Outline each blood parasite and name the species.
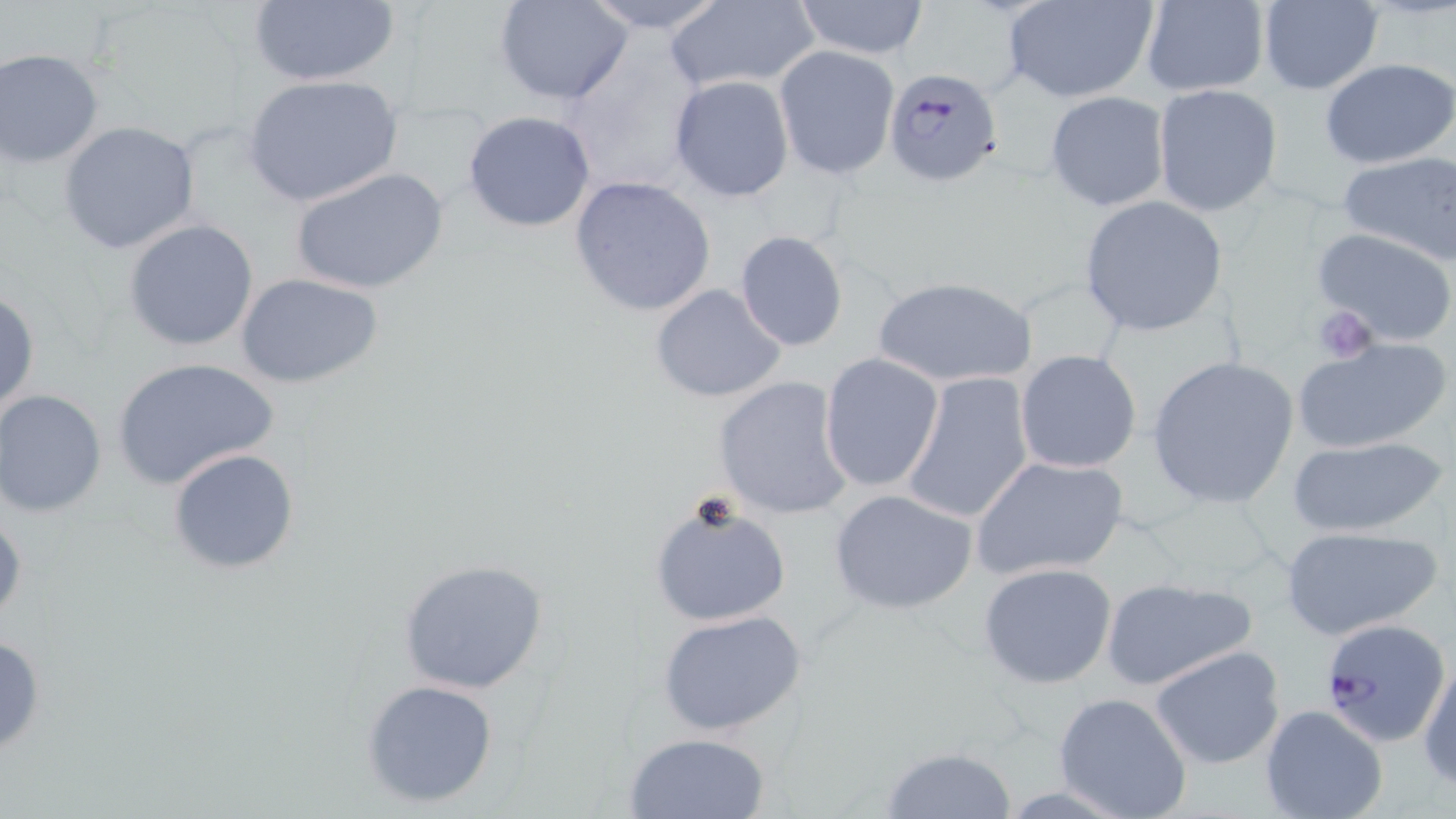

Approximate bounding boxes as (x1,y1)-(x2,y2) corner pairs in pixels.
Plasmodium falciparum-infected red blood cells: (882,66)-(1005,189), (1318,615)-(1449,745).
No Plasmodium ovale, Plasmodium malariae, Plasmodium vivax, Babesia divergens, or Trypanosoma brucei observed.

Uninfected red blood cell locations: (247,0)-(400,88), (574,0)-(731,33), (793,0)-(931,60), (1003,0)-(1157,103), (1139,0)-(1271,96), (496,1)-(634,105), (1256,1)-(1384,94), (663,2)-(821,91), (772,45)-(901,180), (1,48)-(106,169), (1320,57)-(1456,169), (242,73)-(404,210), (669,75)-(795,202), (1151,83)-(1284,218), (1044,92)-(1169,211), (463,109)-(597,233), (58,120)-(202,255), (1337,150)-(1456,265), (293,165)-(450,297), (568,175)-(716,318), (1078,196)-(1230,338), (122,220)-(261,353), (1312,226)-(1456,348), (733,229)-(849,352), (234,272)-(385,389), (871,275)-(1037,389), (649,283)-(787,404), (1,290)-(39,417), (1292,337)-(1450,455), (1015,348)-(1142,473), (818,354)-(944,492), (1146,354)-(1300,510), (110,357)-(278,490), (901,370)-(1036,525), (713,375)-(853,521), (0,389)-(108,518), (1285,435)-(1449,537), (167,448)-(301,575), (970,454)-(1128,583), (828,488)-(979,615), (648,497)-(791,627), (1,500)-(27,628), (1279,526)-(1444,643), (395,558)-(552,695), (977,562)-(1118,688), (1099,575)-(1259,691), (658,608)-(811,738), (1150,644)-(1288,770), (1417,655)-(1455,789), (360,678)-(497,809), (1051,691)-(1193,819), (1260,704)-(1386,819), (622,731)-(772,818), (877,745)-(1019,819). Platelet locations: (1313,304)-(1378,366). Slide-level diagnosis: Plasmodium falciparum. Light microscopy. Thin blood film. 1000x magnification. Image is 1456×819 pixels. May-Grünwald-Giemsa stain. One field of a larger specimen.